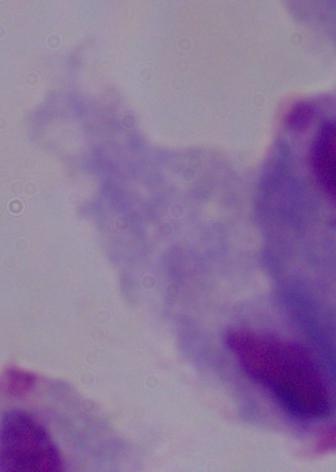
magnification = 1000x
modality = micrograph
identification = trichomonad